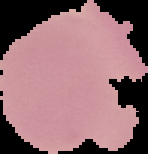

Summary:
  - Image size: 148×154 pixels
  - Preparation: thin blood smear
  - Result: no malaria parasites detected
  - Image type: segmented cell region with the area outside set to black